Outline each blood parasite and name the species.
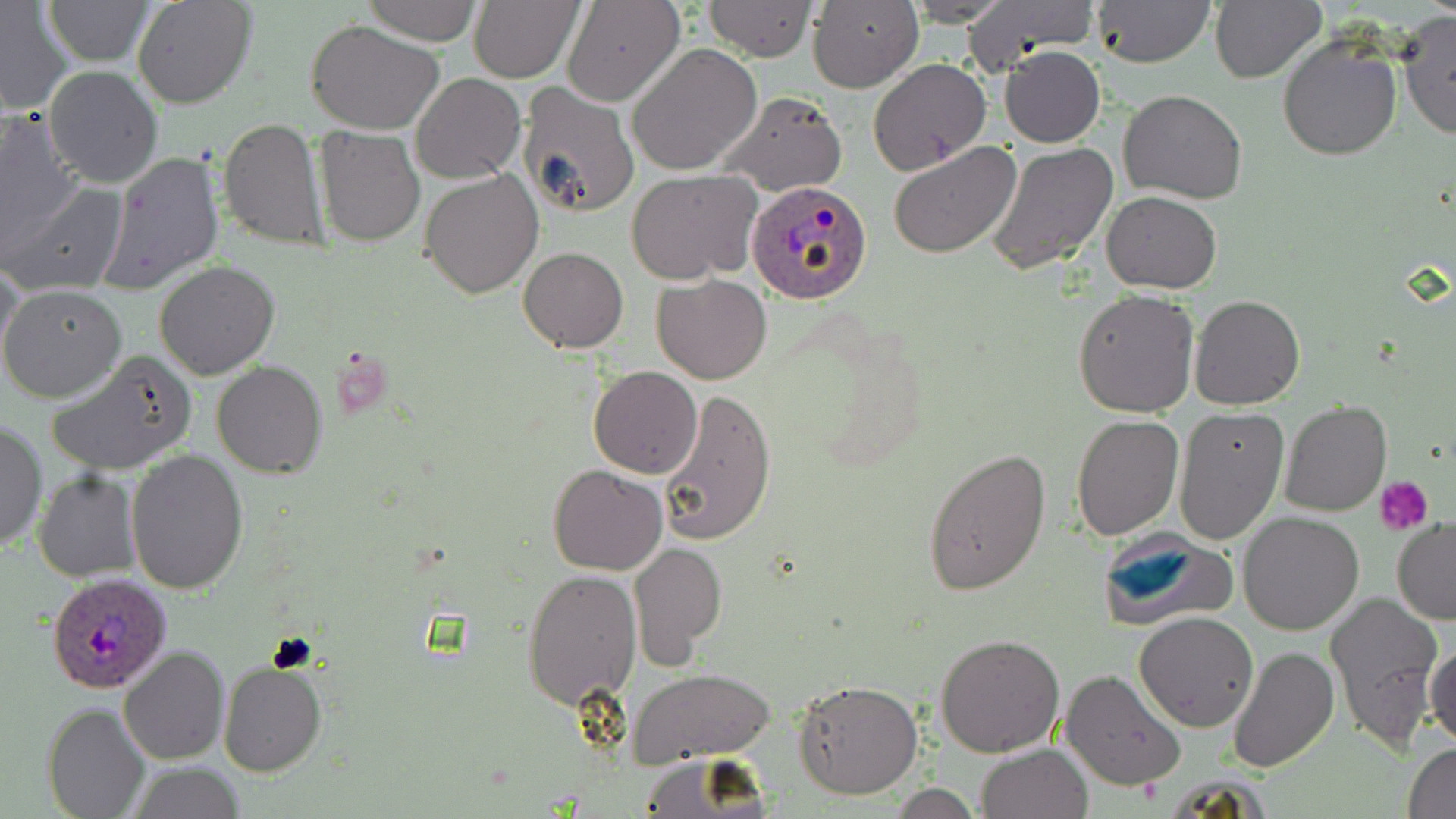
Approximate bounding boxes as [x1, y1, x2, y2] in pixels.
Plasmodium ovale-infected red blood cells: [746, 180, 874, 305], [46, 571, 173, 694].
No Plasmodium falciparum, Plasmodium malariae, Plasmodium vivax, Babesia divergens, or Trypanosoma brucei observed.

Platelet locations: [1375, 476, 1433, 534]. Uninfected red blood cell locations: [43, 0, 152, 65], [132, 0, 255, 109], [365, 0, 481, 45], [904, 0, 1013, 25], [962, 0, 1098, 72], [1093, 0, 1213, 68], [1210, 0, 1324, 82], [702, 1, 818, 61], [807, 1, 924, 93], [470, 2, 582, 82], [563, 2, 684, 108], [0, 4, 74, 113], [1398, 11, 1456, 141], [307, 20, 444, 133], [1277, 35, 1402, 160], [628, 43, 763, 175], [1000, 45, 1105, 148], [868, 59, 991, 175], [43, 65, 163, 188], [410, 72, 525, 184], [516, 82, 638, 220], [719, 90, 846, 195], [1119, 91, 1247, 204], [0, 111, 85, 264], [218, 116, 330, 250], [315, 125, 424, 247], [887, 142, 1021, 259], [986, 143, 1117, 277], [96, 152, 225, 295], [420, 169, 543, 297], [626, 169, 762, 284], [3, 180, 130, 297], [1100, 191, 1222, 293], [518, 246, 628, 352], [1, 257, 23, 364], [154, 260, 280, 380], [652, 275, 772, 385], [1, 284, 127, 403], [1074, 289, 1199, 417], [1189, 293, 1305, 410], [46, 351, 197, 477], [213, 360, 327, 478], [588, 365, 703, 479], [656, 390, 778, 545], [1281, 400, 1392, 516], [1172, 407, 1288, 545], [1071, 413, 1183, 540], [0, 420, 47, 551], [923, 448, 1052, 596], [127, 450, 248, 595], [549, 464, 669, 576], [34, 470, 140, 581], [1238, 511, 1365, 634], [1391, 519, 1456, 624], [1097, 528, 1238, 630], [628, 541, 728, 666], [522, 567, 639, 710], [1326, 590, 1446, 755], [1134, 611, 1258, 731], [935, 634, 1065, 756], [1428, 640, 1456, 749], [1227, 645, 1340, 773], [118, 646, 230, 766], [218, 658, 327, 777], [630, 669, 776, 763], [1060, 669, 1185, 793], [794, 679, 923, 800], [42, 702, 150, 819], [975, 742, 1092, 819], [1405, 743, 1456, 818], [634, 755, 768, 818], [124, 763, 247, 819], [886, 784, 986, 818]. Slide-level diagnosis: Plasmodium ovale. Thin blood film. May-Grünwald-Giemsa stain. Single field of view. 1000x magnification. Image is 1456×819 pixels. Light microscopy.